Describe the morphology of the red blood cells.
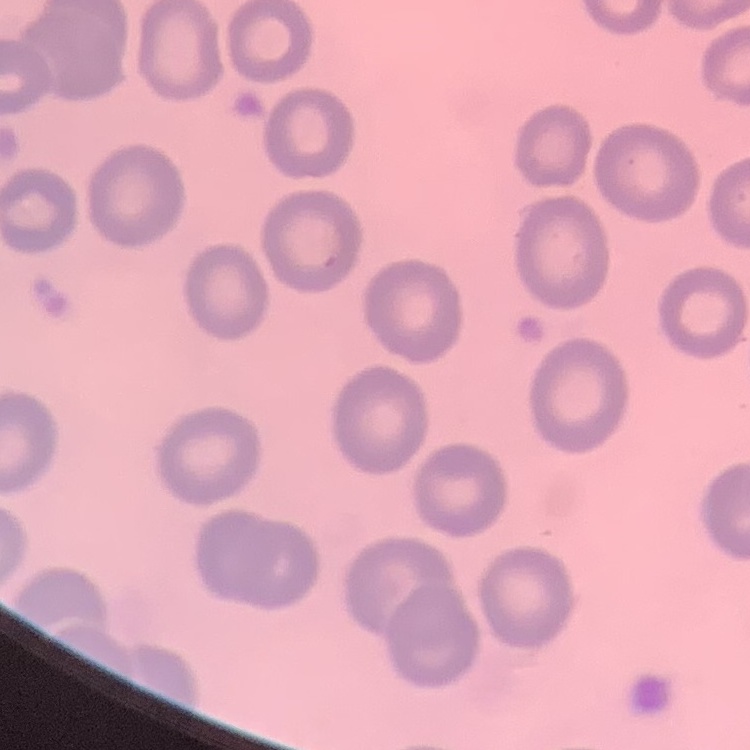

They show no rouleaux formation.

image type = one tile cut from a larger photomicrograph
stain = Field's or Giemsa
preparation = thin blood smear